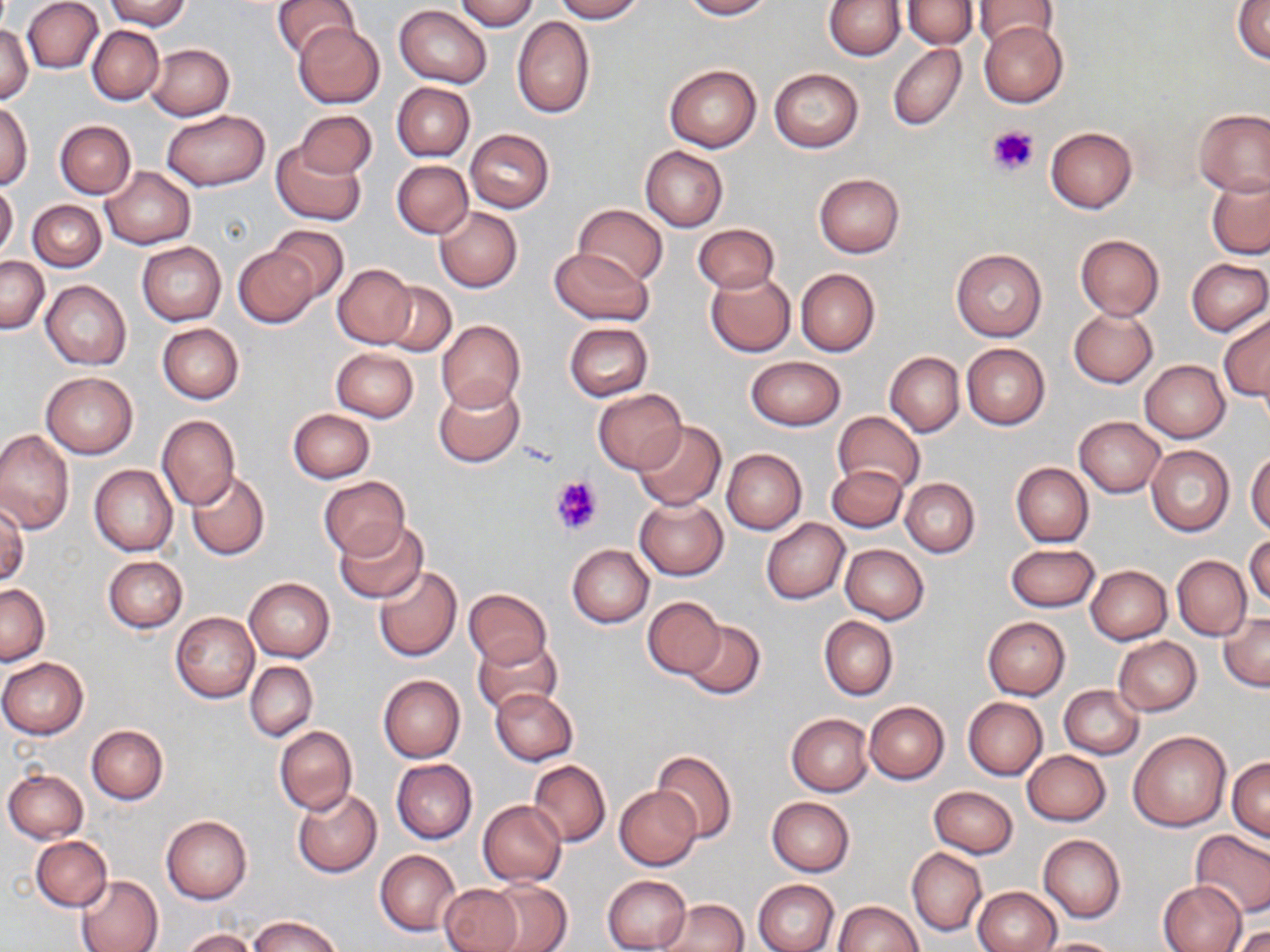

Summary:
  - Coordinate format: approximate bounding boxes as [x1, y1, x2, y2] in pixels
  - Platelet locations: [987, 125, 1038, 177], [552, 475, 602, 533]
  - Uninfected red blood cell locations: [103, 0, 191, 31], [272, 0, 359, 62], [453, 0, 538, 32], [552, 0, 644, 21], [679, 0, 772, 19], [823, 0, 905, 60], [902, 0, 977, 49], [971, 0, 1064, 48], [23, 1, 103, 73], [1233, 1, 1270, 64], [395, 5, 492, 87], [512, 16, 594, 119], [977, 20, 1068, 108], [292, 22, 384, 109], [0, 24, 33, 103], [86, 25, 164, 105], [146, 43, 234, 120], [888, 43, 966, 132], [664, 63, 761, 151], [768, 68, 863, 152], [392, 83, 474, 161], [0, 101, 34, 190], [1193, 108, 1270, 196], [160, 109, 270, 191], [294, 109, 375, 180], [54, 121, 136, 198], [1046, 126, 1137, 213], [465, 129, 554, 212], [272, 141, 366, 224], [640, 146, 728, 231], [392, 160, 473, 238], [100, 168, 194, 249], [813, 173, 906, 258], [1207, 175, 1270, 258], [0, 180, 18, 262], [28, 200, 106, 271], [573, 204, 667, 287], [434, 207, 522, 293], [266, 223, 347, 302], [692, 223, 779, 294], [1074, 234, 1164, 320], [136, 242, 226, 325], [233, 245, 320, 327], [547, 248, 654, 325], [951, 248, 1046, 342], [1, 255, 48, 333], [1186, 258, 1269, 336], [332, 264, 415, 348], [795, 269, 879, 357], [706, 271, 795, 357], [41, 280, 130, 369], [380, 281, 456, 355], [1069, 307, 1157, 388], [1219, 310, 1270, 403], [437, 320, 525, 410], [157, 322, 244, 404], [563, 322, 652, 402], [962, 343, 1050, 429], [331, 348, 419, 421], [885, 351, 964, 436], [747, 356, 844, 430], [1139, 360, 1230, 442], [40, 372, 138, 458], [433, 380, 524, 467], [592, 388, 685, 474], [288, 408, 375, 482], [832, 411, 925, 495], [156, 415, 240, 510], [1074, 416, 1166, 497], [632, 421, 726, 511], [0, 431, 73, 535], [1146, 445, 1234, 536], [1247, 448, 1270, 535], [722, 449, 806, 533], [1011, 462, 1093, 546], [89, 464, 177, 557], [828, 466, 908, 533], [186, 471, 270, 560], [318, 476, 408, 560], [900, 477, 980, 557], [634, 497, 728, 580], [0, 501, 27, 588], [761, 518, 849, 604], [333, 520, 427, 602], [1245, 533, 1270, 610], [839, 543, 928, 623], [1005, 543, 1101, 612], [567, 544, 653, 628], [1172, 555, 1251, 640], [104, 556, 187, 633], [1086, 564, 1172, 643], [373, 565, 462, 662], [245, 577, 334, 662], [1, 583, 49, 665], [462, 589, 552, 669], [642, 597, 728, 679], [171, 611, 259, 703], [1221, 613, 1270, 691], [819, 616, 897, 700], [982, 617, 1070, 700], [680, 620, 765, 700], [471, 637, 563, 717], [1113, 637, 1201, 716], [0, 657, 89, 738], [245, 660, 317, 742], [377, 674, 465, 762], [1059, 684, 1144, 759], [490, 687, 577, 766], [962, 697, 1047, 780], [865, 701, 949, 784], [786, 713, 874, 795], [87, 724, 168, 805], [274, 725, 357, 816], [1129, 731, 1230, 831], [1023, 750, 1110, 827], [653, 751, 737, 842], [1227, 756, 1270, 842], [391, 759, 477, 843], [528, 759, 610, 847], [2, 768, 88, 844], [614, 786, 701, 871], [928, 786, 1017, 857], [292, 787, 382, 877], [767, 796, 855, 876], [761, 797, 844, 952], [478, 800, 566, 886], [161, 814, 252, 903], [1190, 831, 1270, 918], [1039, 834, 1125, 922], [31, 835, 112, 912], [375, 849, 460, 937], [907, 849, 986, 936], [75, 874, 164, 952], [602, 875, 692, 952], [754, 879, 839, 952], [1157, 879, 1247, 951], [484, 880, 572, 952], [437, 883, 522, 952], [974, 887, 1060, 951], [659, 899, 749, 951], [835, 900, 923, 951], [246, 915, 344, 952], [1232, 923, 1270, 951], [180, 929, 257, 952], [1033, 936, 1123, 952]
  - Slide-level diagnosis: no evidence of blood parasites
  - Magnification: 1000x
  - Stain: May-Grünwald-Giemsa
  - Preparation: thin blood film
  - Modality: light microscopy
  - Field of view: one of a larger specimen
  - Image size: 1270×952 pixels